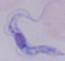
{
  "modality": "micrograph",
  "magnification": "1000x",
  "identification": "trypanosome"
}